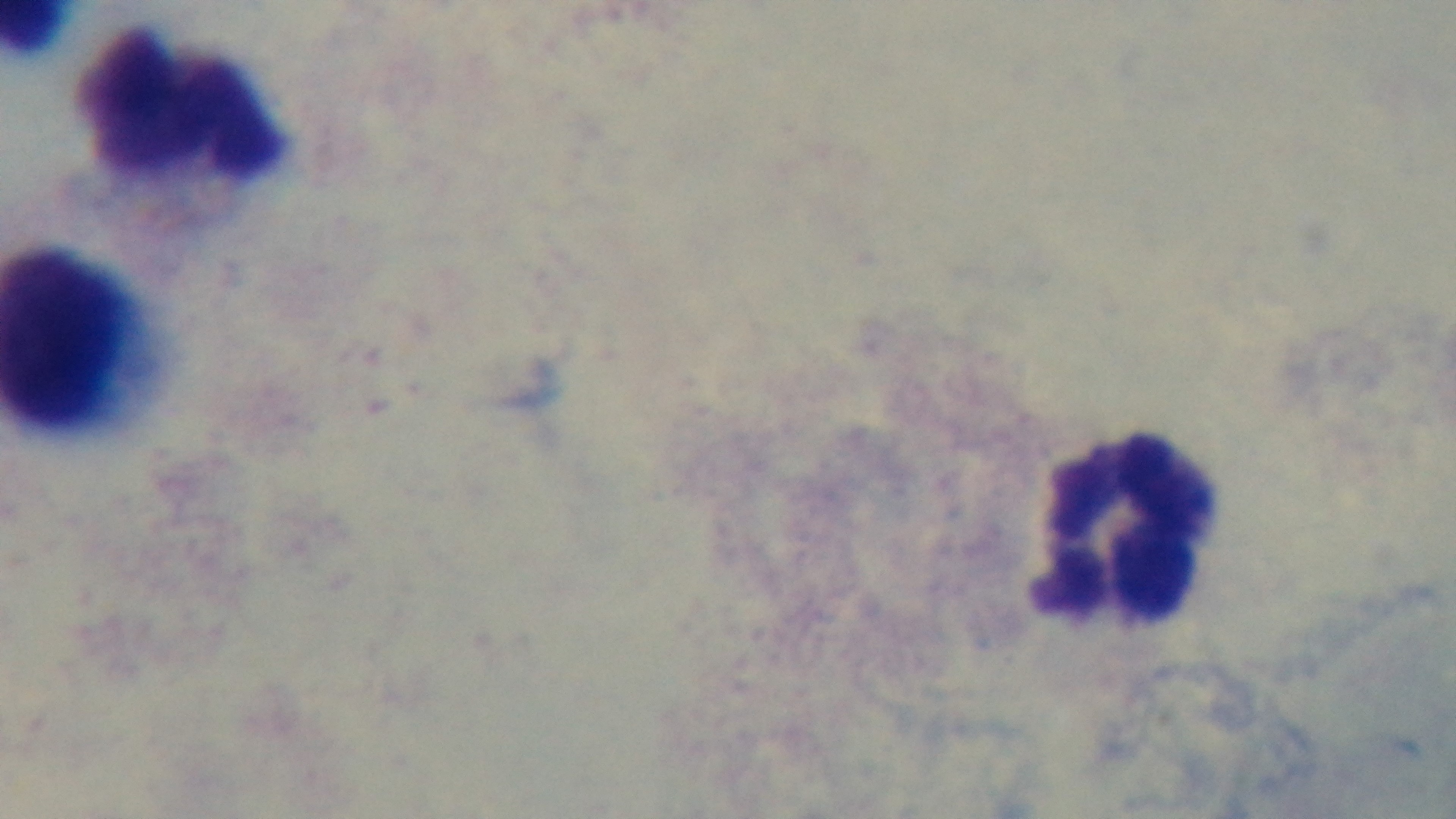

Summary:
  - Modality: light microscopy
  - Field of view: one from the slide
  - Preparation: thick blood film
  - Capture: mounted 4K digital camera
  - Stain: Giemsa
  - Malaria status: negative
  - Objective: 100x oil immersion